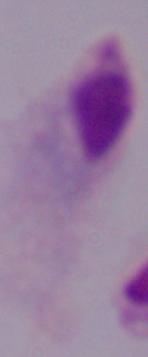

Captured at 1000x magnification. A trichomonad is seen. Micrograph.